Give the extent of all Plasmodium vivax-infected red blood cells.
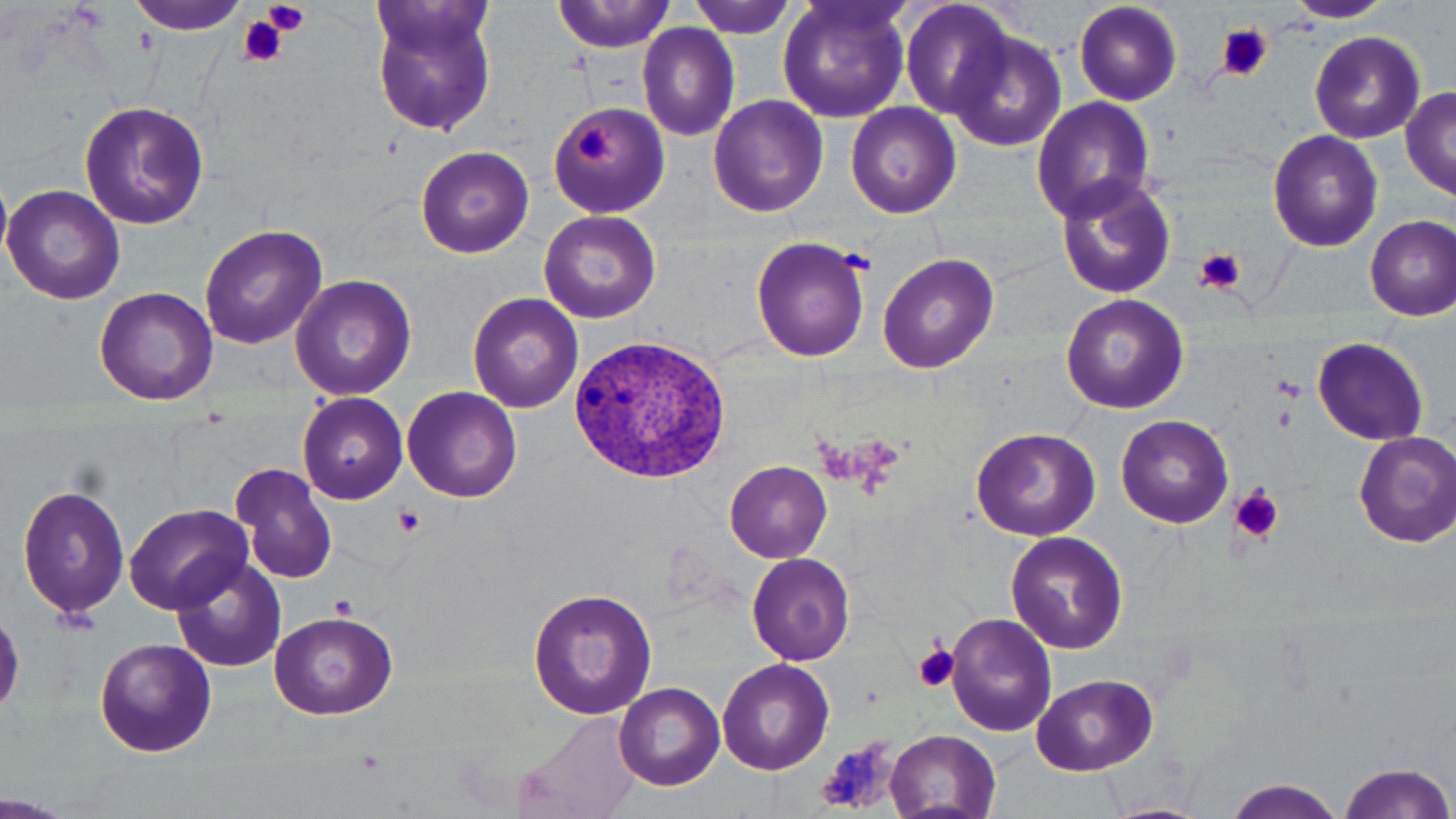
Approximate bounding boxes as named x1/y1/x2/y2 corners in pixels.
Plasmodium vivax-infected red blood cells: (x1=565, y1=332, x2=735, y2=486).

Platelet locations: (x1=263, y1=0, x2=310, y2=33), (x1=238, y1=16, x2=289, y2=68), (x1=1217, y1=25, x2=1271, y2=82), (x1=575, y1=126, x2=615, y2=166), (x1=1193, y1=246, x2=1248, y2=297), (x1=1231, y1=484, x2=1284, y2=543), (x1=391, y1=505, x2=425, y2=539), (x1=330, y1=594, x2=358, y2=620), (x1=911, y1=643, x2=960, y2=695), (x1=815, y1=737, x2=900, y2=813). Uninfected red blood cell locations: (x1=127, y1=0, x2=252, y2=35), (x1=365, y1=0, x2=500, y2=138), (x1=554, y1=0, x2=674, y2=53), (x1=686, y1=0, x2=802, y2=38), (x1=899, y1=0, x2=1016, y2=121), (x1=1071, y1=0, x2=1184, y2=106), (x1=775, y1=1, x2=913, y2=123), (x1=1283, y1=1, x2=1396, y2=23), (x1=637, y1=24, x2=740, y2=142), (x1=945, y1=29, x2=1068, y2=151), (x1=1310, y1=30, x2=1425, y2=142), (x1=1400, y1=87, x2=1456, y2=199), (x1=707, y1=94, x2=829, y2=217), (x1=1032, y1=98, x2=1156, y2=221), (x1=546, y1=99, x2=669, y2=218), (x1=81, y1=101, x2=206, y2=229), (x1=846, y1=103, x2=961, y2=218), (x1=1267, y1=130, x2=1383, y2=252), (x1=414, y1=145, x2=535, y2=258), (x1=1055, y1=175, x2=1177, y2=301), (x1=0, y1=180, x2=12, y2=263), (x1=1, y1=184, x2=126, y2=304), (x1=539, y1=210, x2=660, y2=323), (x1=1364, y1=214, x2=1455, y2=319), (x1=199, y1=224, x2=328, y2=352), (x1=749, y1=235, x2=871, y2=362), (x1=879, y1=252, x2=999, y2=374), (x1=289, y1=275, x2=417, y2=402), (x1=93, y1=286, x2=218, y2=406), (x1=467, y1=292, x2=583, y2=412), (x1=1060, y1=293, x2=1188, y2=413), (x1=1311, y1=336, x2=1430, y2=443), (x1=403, y1=387, x2=522, y2=502), (x1=297, y1=392, x2=408, y2=504), (x1=1116, y1=414, x2=1235, y2=529), (x1=970, y1=427, x2=1100, y2=541), (x1=1353, y1=431, x2=1456, y2=548), (x1=725, y1=462, x2=831, y2=561), (x1=231, y1=463, x2=338, y2=584), (x1=18, y1=482, x2=131, y2=621), (x1=124, y1=503, x2=255, y2=615), (x1=1005, y1=531, x2=1128, y2=655), (x1=746, y1=552, x2=857, y2=665), (x1=170, y1=556, x2=288, y2=673), (x1=526, y1=585, x2=657, y2=722), (x1=267, y1=610, x2=399, y2=720), (x1=946, y1=611, x2=1056, y2=737), (x1=92, y1=638, x2=218, y2=758), (x1=717, y1=659, x2=833, y2=774), (x1=1031, y1=673, x2=1157, y2=774), (x1=614, y1=683, x2=725, y2=790), (x1=510, y1=712, x2=642, y2=819), (x1=884, y1=730, x2=1003, y2=817), (x1=1335, y1=760, x2=1454, y2=819), (x1=1221, y1=779, x2=1349, y2=818), (x1=1101, y1=800, x2=1211, y2=819). Slide-level diagnosis: Plasmodium vivax. Captured at 1000x magnification. Optical microscopy. May-Grünwald-Giemsa stain. One field of a larger specimen. Image is 1456×819 pixels. Thin blood film.